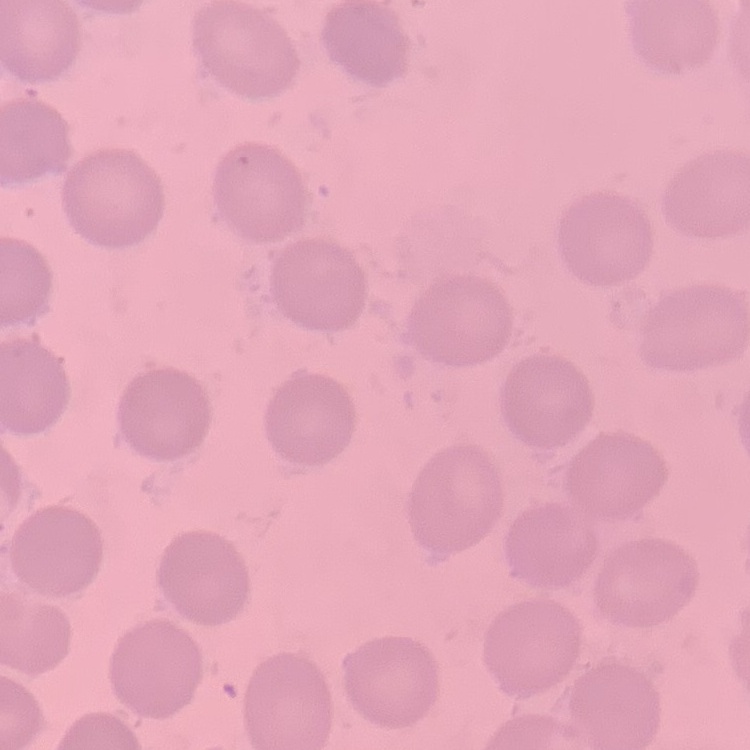

erythrocyte morphology = no rouleaux formation
stain = Field's or Giemsa
image type = square crop of a larger photomicrograph
preparation = thin peripheral smear